Point out each malaria parasite and each leukocyte.
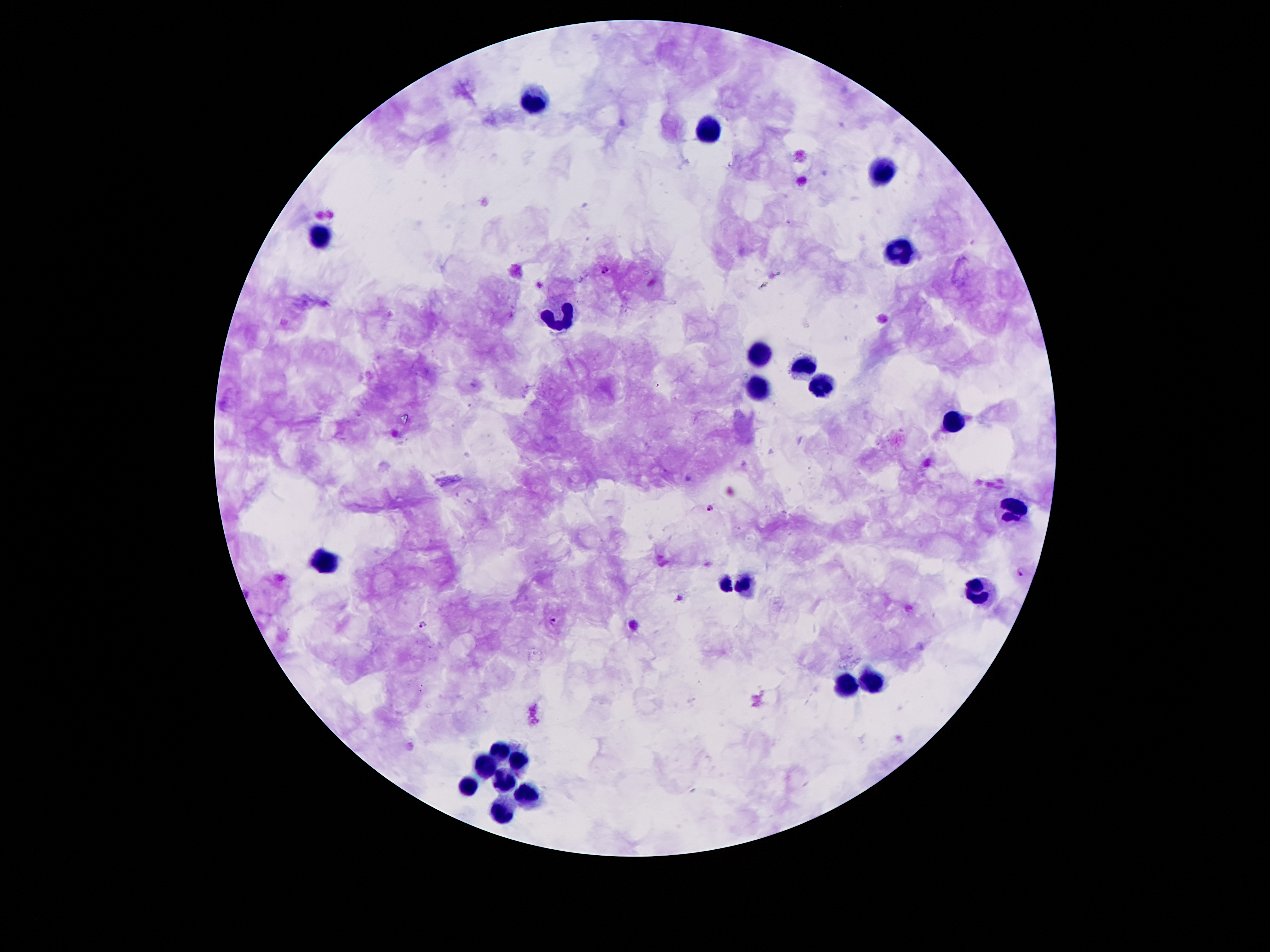
Approximate centers as (x, y) in pixels.
Malaria parasites: (606, 269), (712, 509), (1024, 573), (554, 621), (425, 624).
Leukocytes: (533, 102), (710, 128), (886, 170), (323, 236), (902, 254), (561, 316), (757, 356), (808, 366), (823, 386), (755, 391), (951, 424), (1014, 504), (326, 562), (734, 581), (979, 594), (871, 682), (843, 686), (501, 751), (519, 758), (482, 768), (503, 779), (464, 787), (531, 797), (503, 808).

{
  "capture": "smartphone through the microscope eyepiece",
  "patient_malaria_status": "positive for Plasmodium falciparum",
  "preparation": "thick blood smear",
  "image_size": "1270×952 pixels",
  "field_of_view": "single",
  "stain": "Giemsa",
  "magnification": "100x"
}